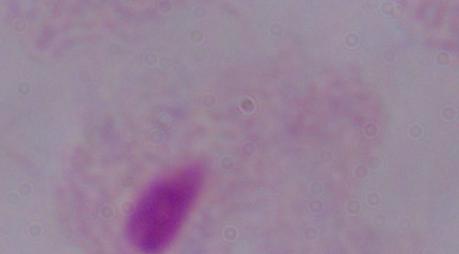 Photomicrograph. Captured at 1000x magnification. A trichomonad is shown.